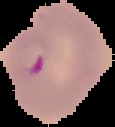

image type = segmented cell region on a black background
preparation = thin blood film
image size = 115×127 pixels
malaria status = parasitized